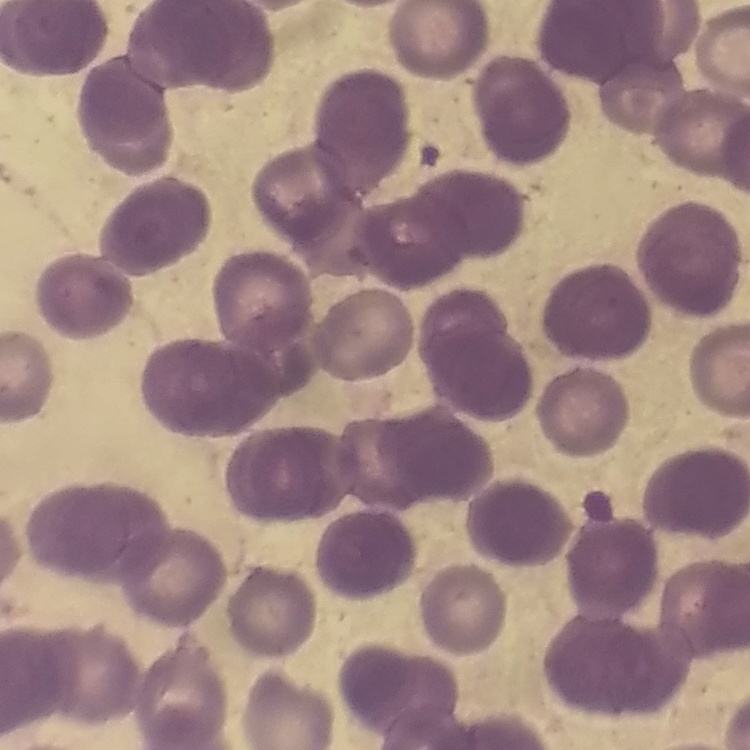
The red blood cells exhibit rouleaux formation. Square crop of a larger photomicrograph. Field's or Giemsa stain. Thin blood film.